Evaluate for Plasmodium parasites.
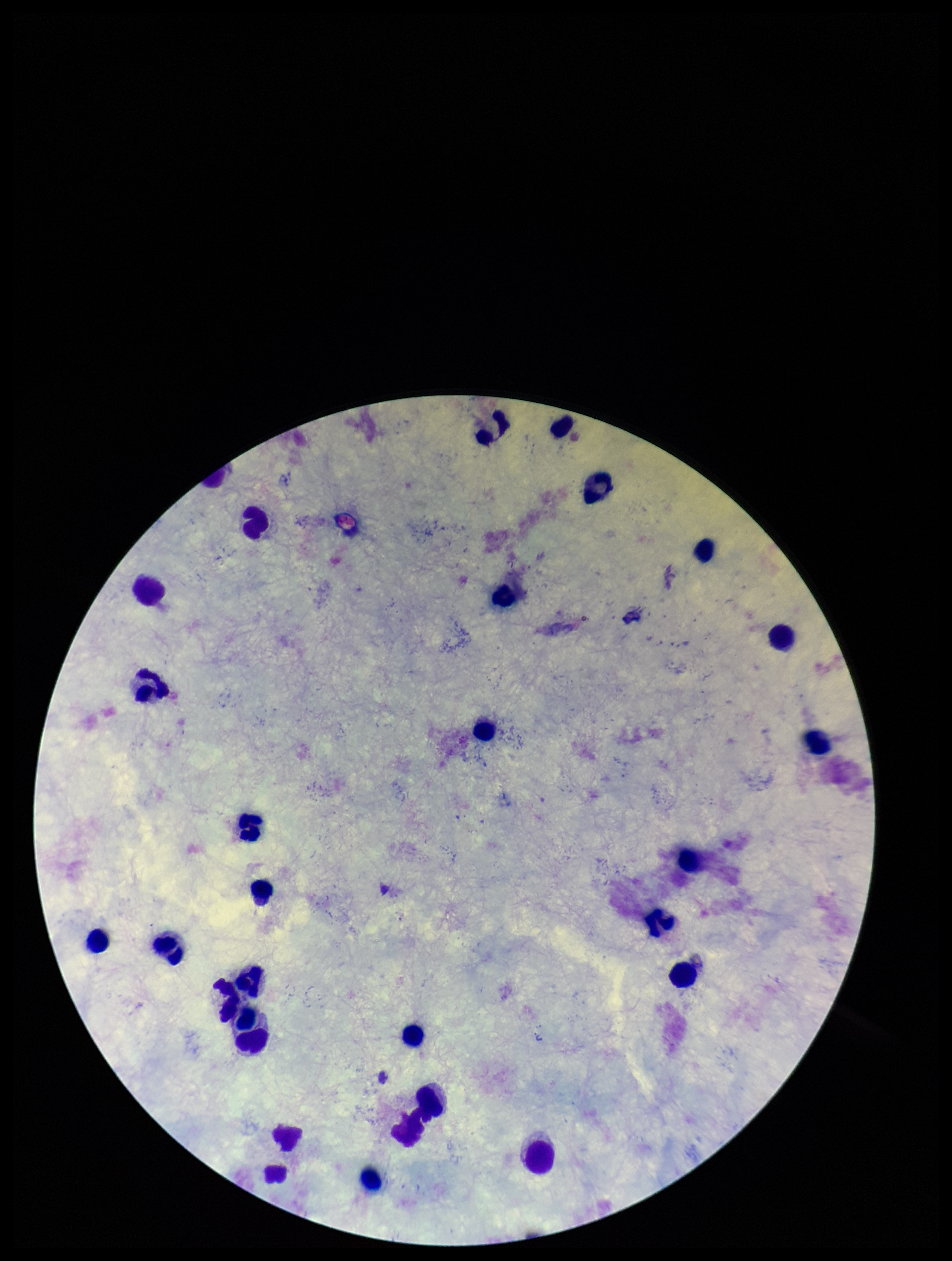

None seen.

Photographed through the microscope eyepiece with a smartphone camera. Leukocyte count: 27. Image is 952×1261 pixels. Patient malaria status: negative. Parasite count: 0. Giemsa stain. Preparation: thick smear. One field from this slide.